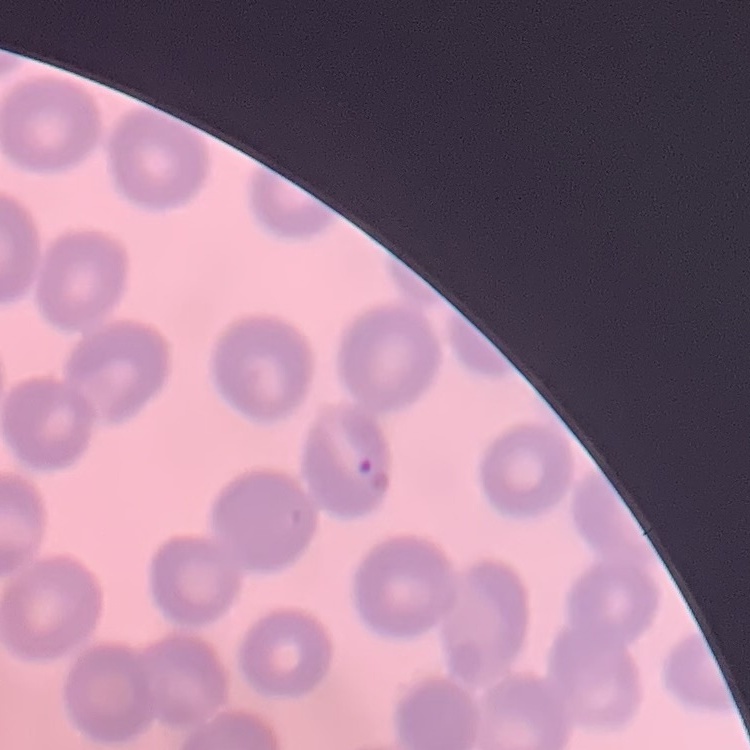

Summary:
  - Red blood cell morphology: no rouleaux formation
  - Image type: square crop of a larger photomicrograph
  - Stain: Field's or Giemsa
  - Preparation: thin peripheral smear